Describe the morphology of the erythrocytes.
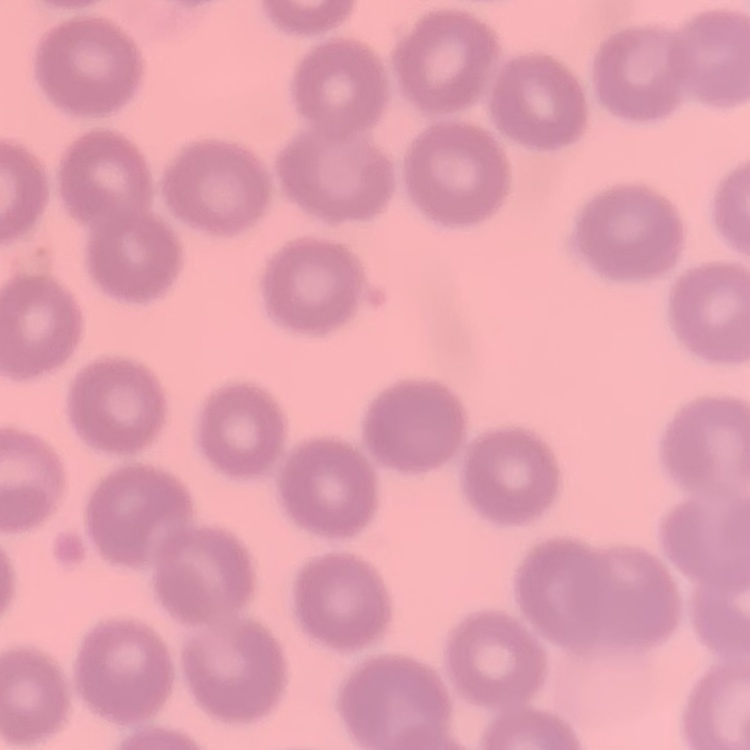

No rouleaux formation.

Summary:
  - Image type: square crop of a larger photomicrograph
  - Preparation: thin peripheral smear
  - Stain: Field's or Giemsa